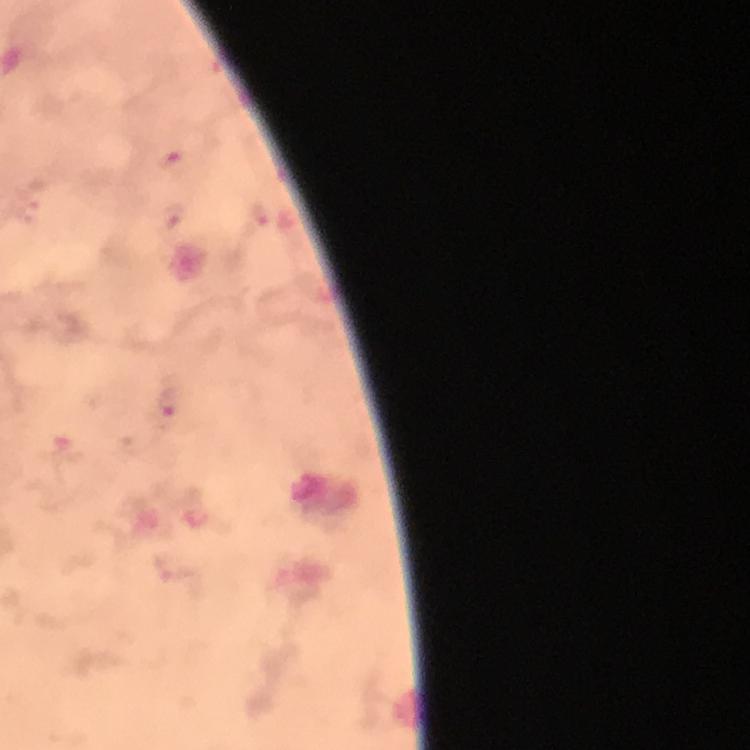

Approximate centers as [x, y] in pixels.
Summary:
  - Malaria parasite locations: [170, 403]
  - Preparation: thick smear
  - Cropped from: one field of view
  - Magnification: 100x
  - Immersion oil: used
  - Capture: smartphone mounted on the microscope
  - Stain: Giemsa
  - Context: from a malaria diagnostic workup
  - Image size: 750×750 pixels